Locate every blood parasite and identify its species.
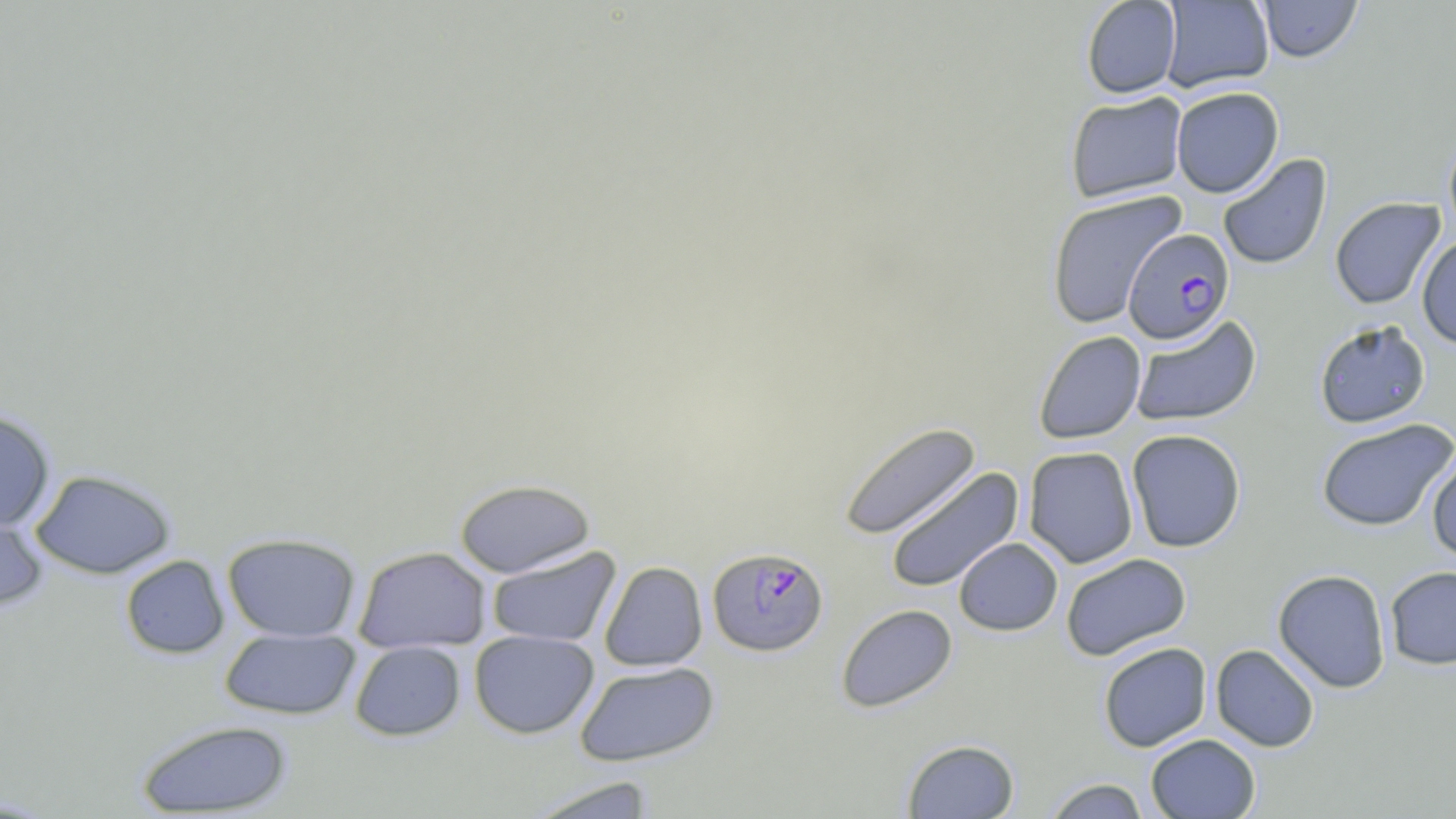

Approximate bounding boxes as (x1,y1)-(x2,y2) corner pairs in pixels.
Plasmodium falciparum-infected red blood cells: (1123,229)-(1235,344), (707,547)-(829,657).
No Plasmodium ovale, Plasmodium malariae, Plasmodium vivax, Babesia divergens, or Trypanosoma brucei observed.

Uninfected red blood cell locations: (1080,0)-(1182,99), (1159,0)-(1275,92), (1257,1)-(1363,63), (1171,86)-(1284,198), (1065,91)-(1188,203), (1443,130)-(1456,247), (1217,154)-(1333,271), (1045,190)-(1186,329), (1329,197)-(1446,310), (1416,235)-(1456,349), (1129,314)-(1262,428), (1314,320)-(1431,428), (1033,330)-(1147,444), (0,409)-(56,531), (1316,418)-(1455,531), (838,421)-(981,540), (1126,428)-(1247,553), (1023,446)-(1139,568), (1426,450)-(1456,563), (884,467)-(1024,593), (30,469)-(176,579), (454,478)-(595,578), (0,506)-(49,612), (222,532)-(361,642), (954,537)-(1063,636), (354,546)-(491,653), (486,546)-(621,648), (1060,553)-(1191,661), (120,554)-(230,659), (599,561)-(708,671), (1384,566)-(1456,669), (1273,569)-(1392,693), (836,604)-(957,712), (219,628)-(361,720), (469,630)-(599,739), (349,640)-(466,741), (1098,641)-(1212,752), (1210,644)-(1320,752), (575,660)-(720,766), (135,719)-(293,817), (1146,733)-(1261,818), (902,739)-(1020,819), (526,775)-(659,819), (1042,777)-(1151,819). Slide-level diagnosis: Plasmodium falciparum. May-Grünwald-Giemsa-stained preparation. Optical microscopy. Image is 1456×819 pixels. Thin blood smear. 1000x magnification. Single field of view.